Point out each leukocyte.
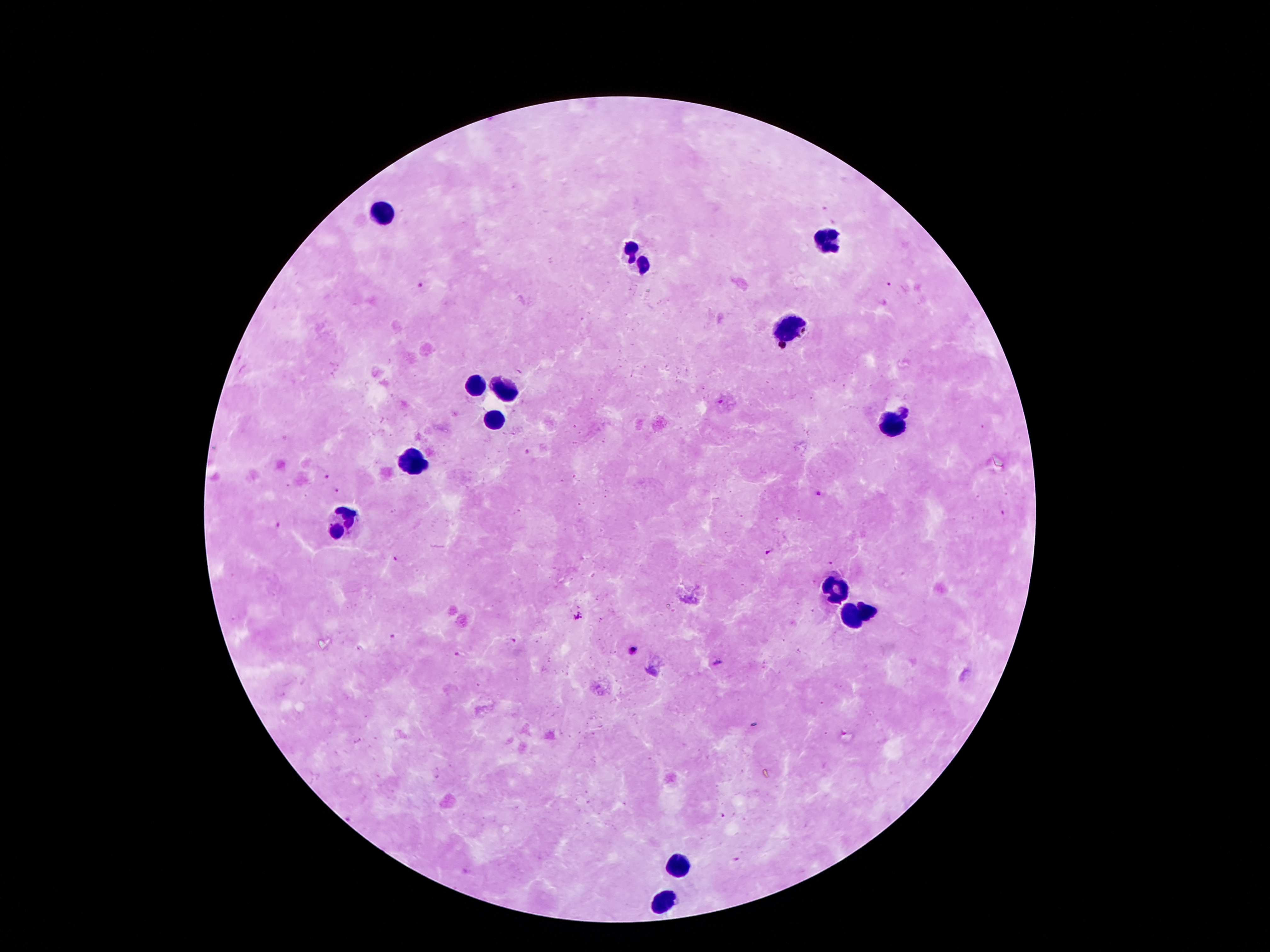
Approximate object centers, in pixels from the top-left corner.
Leukocytes: (x=387, y=213), (x=821, y=240), (x=635, y=261), (x=785, y=326), (x=474, y=383), (x=504, y=390), (x=497, y=420), (x=892, y=420), (x=413, y=461), (x=340, y=513), (x=827, y=586), (x=870, y=612), (x=849, y=614), (x=676, y=867), (x=663, y=901).

Plasmodium parasite locations: (x=889, y=283), (x=422, y=287), (x=903, y=412), (x=527, y=451), (x=325, y=475), (x=337, y=490), (x=818, y=494), (x=279, y=525), (x=770, y=552), (x=396, y=558), (x=831, y=562), (x=577, y=618), (x=391, y=635), (x=515, y=640), (x=632, y=650), (x=457, y=654), (x=719, y=662), (x=722, y=815), (x=737, y=859). Photographed through the microscope eyepiece with a smartphone camera. Giemsa-stained preparation. 100x magnification. Single field of view. Image is 1270×952 pixels. Patient malaria status: positive for Plasmodium falciparum. Thick blood film.